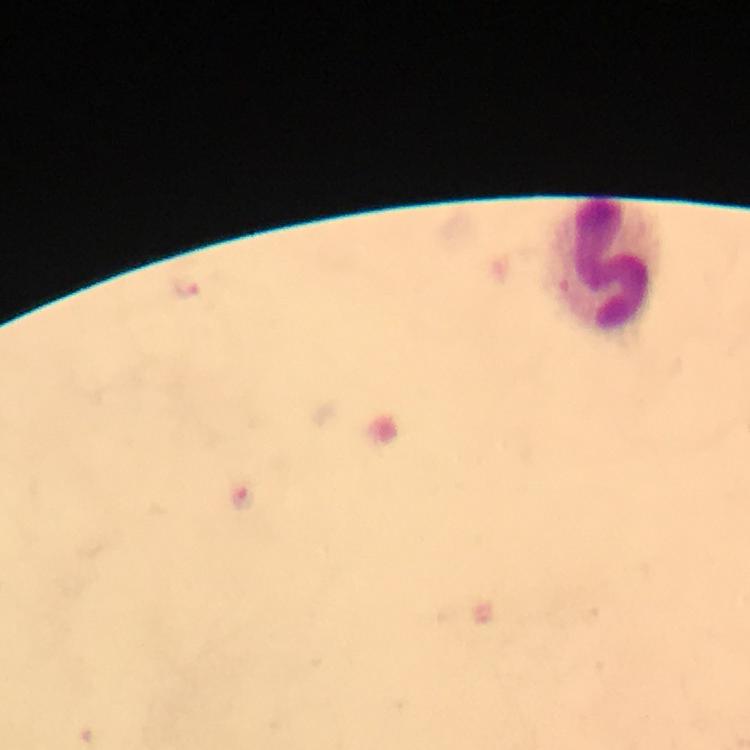
image_size: 750×750 pixels
preparation: thick smear
context: from a malaria diagnostic workup
cropped_from: one field of view
capture: smartphone camera through the microscope
leukocyte_locations: 'approximate centers as (x, y) in pixels: (609, 264)'
stain: Giemsa
immersion_oil: used
magnification: 100x
plasmodium_parasite_locations: 'approximate centers as (x, y) in pixels: (187, 288), (242, 499)'